Name the parasite shown.
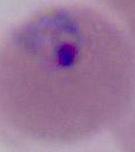

Plasmodium.

magnification: 400x or 1000x
modality: photomicrograph